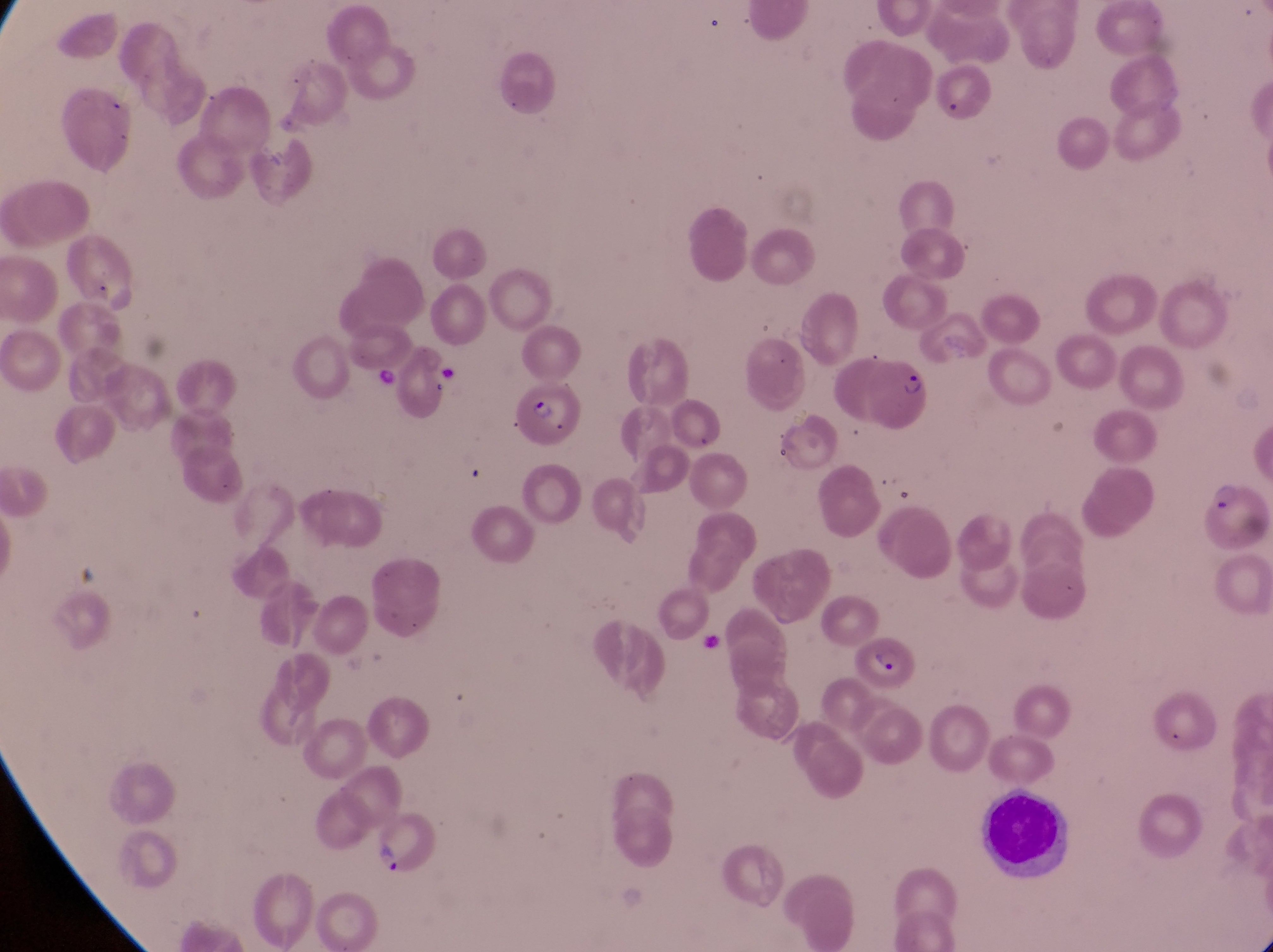

artifact_platelet_like_body_stain_precipitate_or_debris_locations: 'approximate bounding boxes as {left, top, right, bottom} in pixels: {429, 357, 459, 390}, {374, 364, 402, 391}'
country: Uganda
image_size: 1273×952 pixels
preparation: thin blood smear
leukocyte_locations: 'approximate bounding boxes as {left, top, right, bottom} in pixels: {988, 786, 1081, 879}'
field_of_view: single
parasitised_red_blood_cell_locations: 'approximate bounding boxes as {left, top, right, bottom} in pixels: {863, 350, 935, 428}, {511, 379, 583, 447}, {1199, 474, 1268, 556}, {861, 639, 923, 694}'
magnification: 1000x
capture: smartphone photograph through the eyepiece of an Olympus CX-23 microscope
trophozoite_locations: 'approximate bounding boxes as {left, top, right, bottom} in pixels: {369, 839, 404, 881}'